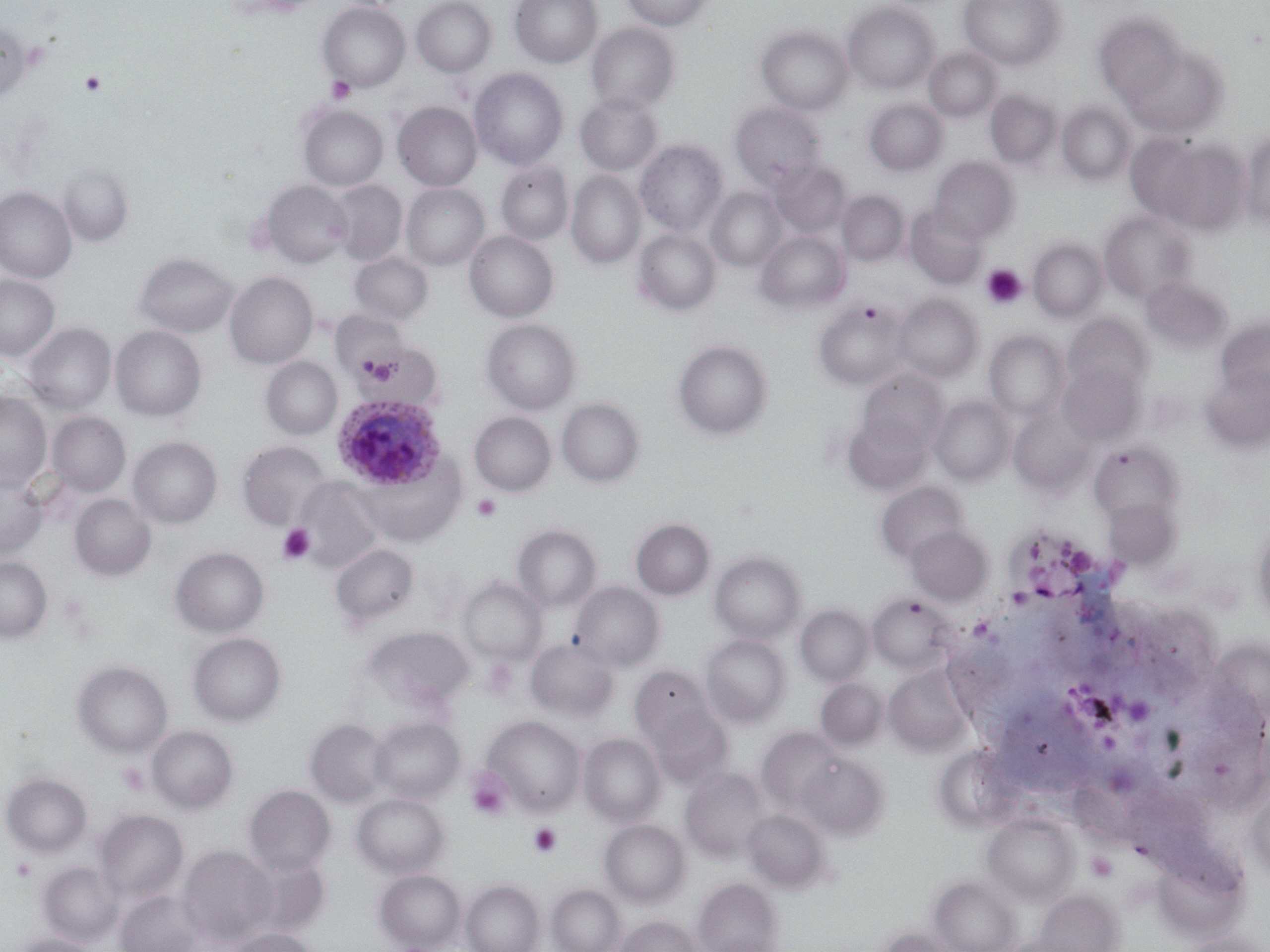
slide-level diagnosis = Plasmodium ovale
platelet locations = approximate bounding boxes as named x1/y1/x2/y2 corners in pixels: (x1=80, y1=70, x2=106, y2=96), (x1=326, y1=77, x2=356, y2=104), (x1=981, y1=263, x2=1028, y2=310), (x1=359, y1=354, x2=398, y2=383), (x1=472, y1=493, x2=502, y2=522), (x1=277, y1=523, x2=315, y2=566), (x1=117, y1=763, x2=151, y2=797), (x1=466, y1=767, x2=513, y2=821), (x1=528, y1=823, x2=562, y2=858), (x1=1086, y1=852, x2=1118, y2=882), (x1=11, y1=858, x2=36, y2=883)
stain = May-Grünwald-Giemsa
magnification = 1000x
Plasmodium ovale-infected red blood cell locations = approximate bounding boxes as named x1/y1/x2/y2 corners in pixels: (x1=332, y1=395, x2=447, y2=492)
field of view = single
modality = optical microscopy
uninfected red blood cell locations = approximate bounding boxes as named x1/y1/x2/y2 corners in pixels: (x1=411, y1=0, x2=496, y2=77), (x1=510, y1=0, x2=603, y2=68), (x1=622, y1=0, x2=712, y2=31), (x1=959, y1=0, x2=1064, y2=70), (x1=317, y1=2, x2=410, y2=92), (x1=842, y1=2, x2=940, y2=93), (x1=1094, y1=13, x2=1184, y2=105), (x1=0, y1=21, x2=33, y2=101), (x1=586, y1=23, x2=678, y2=115), (x1=756, y1=26, x2=853, y2=115), (x1=924, y1=48, x2=1002, y2=122), (x1=1127, y1=48, x2=1228, y2=139), (x1=470, y1=67, x2=568, y2=171), (x1=985, y1=89, x2=1061, y2=168), (x1=575, y1=94, x2=662, y2=176), (x1=863, y1=99, x2=948, y2=176), (x1=393, y1=101, x2=482, y2=191), (x1=730, y1=102, x2=825, y2=191), (x1=1057, y1=103, x2=1136, y2=184), (x1=298, y1=104, x2=388, y2=191), (x1=1241, y1=131, x2=1270, y2=227), (x1=1154, y1=138, x2=1251, y2=235), (x1=635, y1=140, x2=728, y2=238), (x1=928, y1=156, x2=1019, y2=244), (x1=770, y1=160, x2=853, y2=238), (x1=497, y1=161, x2=573, y2=245), (x1=58, y1=164, x2=134, y2=246), (x1=567, y1=171, x2=645, y2=270), (x1=262, y1=180, x2=353, y2=268), (x1=329, y1=180, x2=407, y2=266), (x1=401, y1=184, x2=489, y2=271), (x1=0, y1=187, x2=76, y2=283), (x1=707, y1=188, x2=787, y2=271), (x1=837, y1=190, x2=908, y2=266), (x1=905, y1=206, x2=988, y2=289), (x1=1099, y1=210, x2=1197, y2=305), (x1=634, y1=229, x2=720, y2=315), (x1=756, y1=230, x2=850, y2=314), (x1=465, y1=231, x2=558, y2=322), (x1=1029, y1=238, x2=1108, y2=323), (x1=350, y1=252, x2=433, y2=325), (x1=135, y1=253, x2=237, y2=338), (x1=225, y1=271, x2=318, y2=369), (x1=0, y1=275, x2=59, y2=360), (x1=1141, y1=277, x2=1233, y2=353), (x1=893, y1=294, x2=982, y2=383), (x1=814, y1=298, x2=910, y2=390), (x1=1063, y1=315, x2=1153, y2=395), (x1=482, y1=318, x2=581, y2=415), (x1=1216, y1=319, x2=1270, y2=396), (x1=26, y1=323, x2=116, y2=414), (x1=39, y1=324, x2=121, y2=495), (x1=110, y1=325, x2=206, y2=422), (x1=985, y1=331, x2=1069, y2=420), (x1=673, y1=340, x2=772, y2=439), (x1=357, y1=343, x2=443, y2=409), (x1=261, y1=357, x2=342, y2=440), (x1=1057, y1=362, x2=1144, y2=446), (x1=1200, y1=367, x2=1270, y2=452), (x1=857, y1=369, x2=949, y2=457), (x1=0, y1=393, x2=51, y2=492), (x1=930, y1=396, x2=1015, y2=484), (x1=557, y1=398, x2=644, y2=487), (x1=1008, y1=408, x2=1093, y2=493), (x1=47, y1=411, x2=130, y2=496), (x1=470, y1=412, x2=555, y2=496), (x1=844, y1=418, x2=933, y2=497), (x1=128, y1=437, x2=222, y2=529), (x1=1088, y1=440, x2=1182, y2=523), (x1=237, y1=441, x2=331, y2=531), (x1=354, y1=452, x2=467, y2=546), (x1=0, y1=473, x2=47, y2=560), (x1=294, y1=478, x2=382, y2=575), (x1=876, y1=481, x2=968, y2=564), (x1=70, y1=494, x2=156, y2=580), (x1=1103, y1=498, x2=1178, y2=568), (x1=631, y1=518, x2=715, y2=599), (x1=513, y1=524, x2=601, y2=613), (x1=1251, y1=524, x2=1270, y2=622), (x1=906, y1=525, x2=992, y2=605), (x1=330, y1=543, x2=419, y2=629), (x1=171, y1=547, x2=268, y2=637), (x1=710, y1=551, x2=804, y2=643), (x1=0, y1=557, x2=52, y2=642), (x1=459, y1=577, x2=547, y2=665), (x1=570, y1=582, x2=664, y2=671), (x1=868, y1=592, x2=955, y2=672), (x1=796, y1=605, x2=873, y2=686), (x1=362, y1=625, x2=473, y2=710), (x1=188, y1=632, x2=286, y2=726), (x1=701, y1=635, x2=790, y2=726), (x1=527, y1=639, x2=618, y2=721), (x1=73, y1=660, x2=172, y2=758), (x1=885, y1=665, x2=971, y2=754), (x1=630, y1=666, x2=714, y2=746), (x1=816, y1=679, x2=886, y2=749), (x1=646, y1=707, x2=733, y2=787), (x1=483, y1=715, x2=586, y2=815), (x1=369, y1=716, x2=464, y2=804), (x1=306, y1=719, x2=387, y2=807), (x1=147, y1=725, x2=238, y2=813), (x1=757, y1=728, x2=844, y2=813), (x1=579, y1=733, x2=665, y2=826), (x1=797, y1=753, x2=887, y2=838), (x1=680, y1=766, x2=771, y2=861), (x1=2, y1=773, x2=91, y2=857), (x1=245, y1=785, x2=335, y2=875), (x1=1246, y1=787, x2=1270, y2=880), (x1=352, y1=793, x2=449, y2=878), (x1=94, y1=809, x2=188, y2=904), (x1=743, y1=809, x2=829, y2=892), (x1=983, y1=813, x2=1079, y2=903), (x1=600, y1=819, x2=689, y2=906), (x1=179, y1=845, x2=277, y2=946), (x1=246, y1=854, x2=329, y2=937), (x1=39, y1=863, x2=121, y2=945), (x1=375, y1=869, x2=465, y2=951), (x1=932, y1=877, x2=1020, y2=952), (x1=693, y1=878, x2=780, y2=952), (x1=461, y1=879, x2=544, y2=952), (x1=547, y1=884, x2=625, y2=952), (x1=1035, y1=889, x2=1122, y2=952), (x1=117, y1=891, x2=203, y2=952), (x1=615, y1=915, x2=701, y2=952), (x1=878, y1=927, x2=959, y2=952), (x1=227, y1=928, x2=318, y2=952), (x1=1177, y1=931, x2=1270, y2=952), (x1=12, y1=935, x2=98, y2=952)
image size = 1270×952 pixels
preparation = thin blood smear